Mark where platelets are.
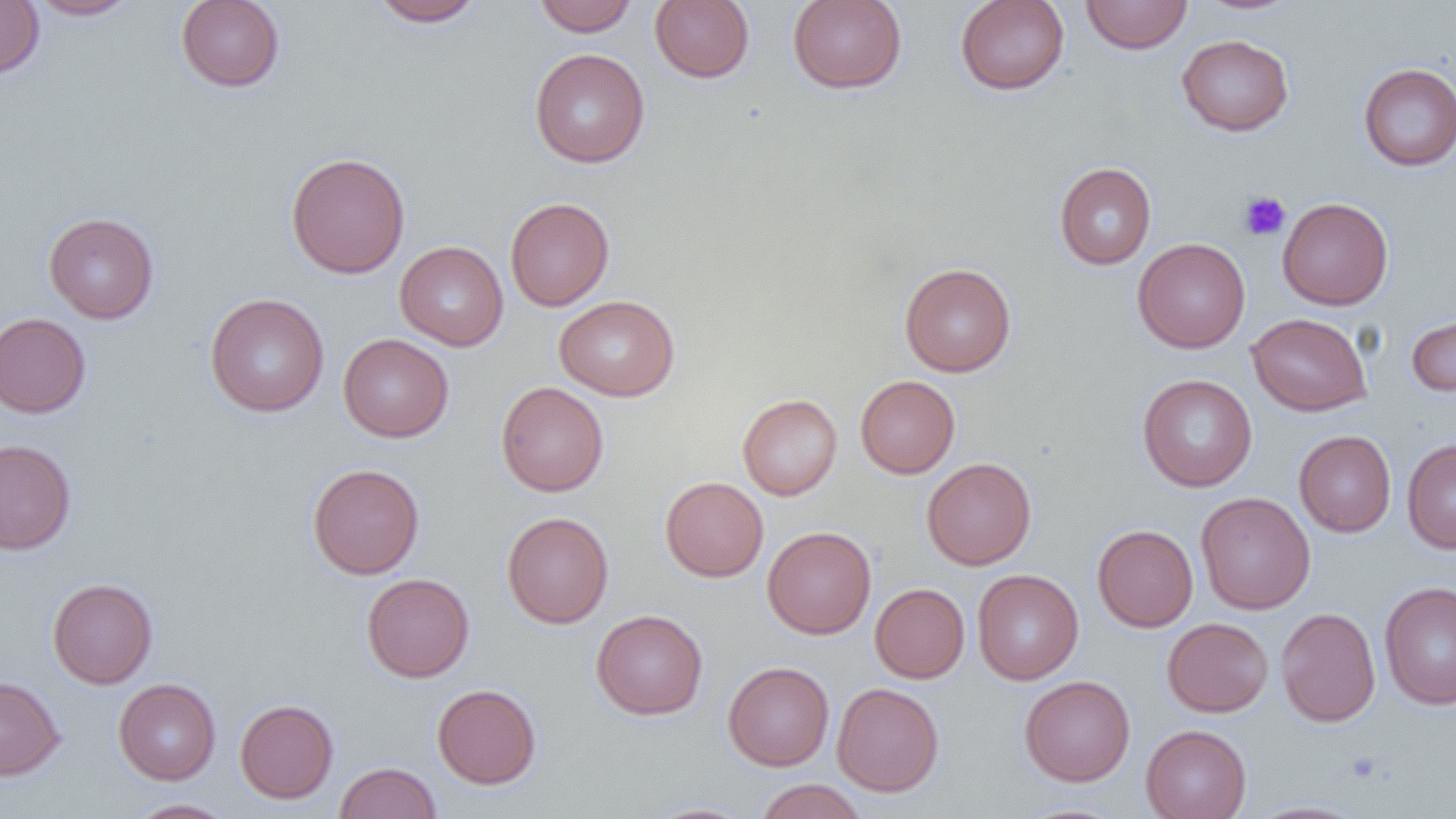
Approximate bounding boxes as (x1,y1)-(x2,y2) corner pairs in pixels.
Platelets: (1239,191)-(1291,241).

Uninfected red blood cell locations: (0,0)-(44,79), (26,0)-(139,20), (175,0)-(285,92), (369,0)-(485,27), (532,0)-(638,36), (650,0)-(754,83), (788,0)-(907,93), (955,0)-(1069,95), (1080,0)-(1193,54), (1192,0)-(1305,16), (1176,34)-(1293,136), (530,48)-(650,168), (1358,63)-(1456,171), (285,152)-(411,278), (1054,162)-(1156,270), (505,197)-(615,311), (1278,197)-(1394,310), (43,212)-(159,324), (1132,238)-(1250,353), (395,241)-(508,351), (899,262)-(1016,377), (204,293)-(329,417), (554,295)-(680,401), (1405,310)-(1456,397), (0,312)-(91,418), (1247,313)-(1372,416), (339,333)-(454,442), (1137,374)-(1257,492), (855,375)-(960,478), (496,381)-(609,496), (737,394)-(842,500), (1294,430)-(1396,537), (0,439)-(76,555), (1402,439)-(1456,554), (921,457)-(1036,570), (307,463)-(424,579), (660,476)-(769,582), (1195,492)-(1315,614), (502,511)-(614,628), (1092,524)-(1199,632), (762,526)-(876,639), (972,569)-(1083,685), (361,573)-(475,683), (47,578)-(158,689), (1379,581)-(1456,709), (870,583)-(970,683), (1276,607)-(1381,726), (591,609)-(708,719), (1162,617)-(1273,717), (723,661)-(834,770), (0,675)-(65,780), (1019,675)-(1135,786), (113,678)-(221,784), (832,682)-(944,797), (432,683)-(541,789), (235,699)-(338,803), (1141,724)-(1251,819), (335,762)-(441,819), (754,779)-(868,818), (125,799)-(238,819), (641,802)-(756,819). Slide-level diagnosis: negative for blood parasites. Image is 1456×819 pixels. Optical microscopy. One field of a larger specimen. Captured at 1000x magnification. Thin blood smear.